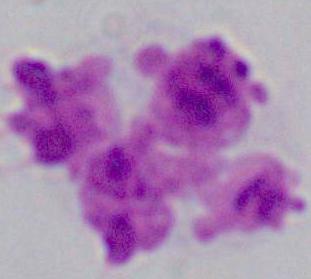

modality = micrograph
magnification = 1000x
identification = leukocyte